Locate every leukocyte (white blood cell).
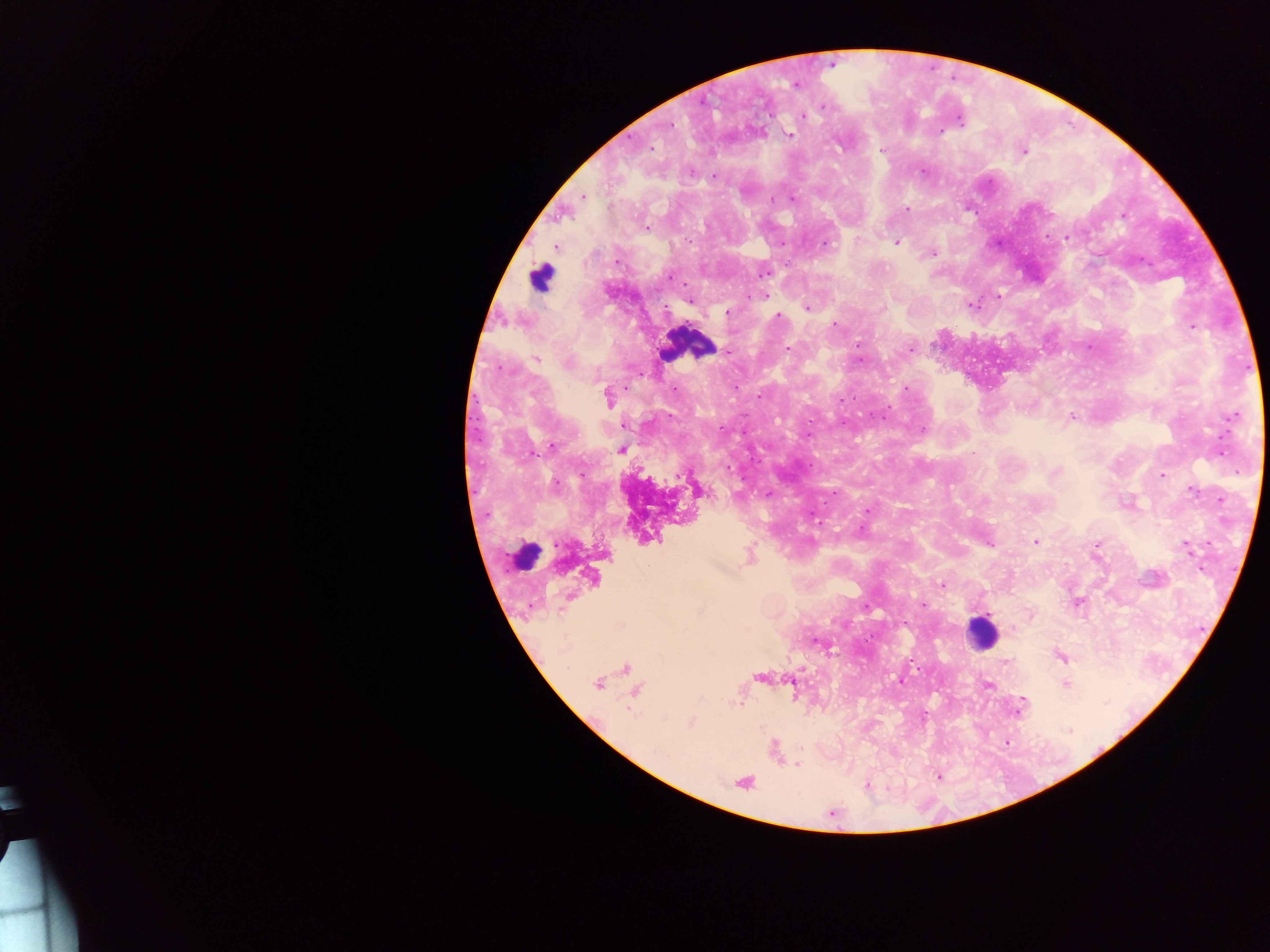
Approximate centers as {x, y} in pixels.
Leukocytes: {540, 278}, {687, 344}, {524, 556}, {981, 631}.

image_size: 1270×952 pixels
capture: mobile-phone photograph through a microscope
preparation: thick blood film
country: Ghana
field_of_view: single
plasmodium_parasite_locations: 'approximate centers as {x, y} in pixels: {830, 65}, {795, 85}, {823, 107}, {803, 116}, {959, 119}, {669, 125}, {939, 131}, {788, 133}, {650, 148}, {882, 149}, {1023, 151}, {713, 177}, {583, 195}, {792, 199}, {907, 209}, {1123, 216}, {646, 227}, {1066, 237}, {897, 242}, {556, 246}, {931, 252}, {765, 295}, {997, 297}, {689, 299}, {971, 305}, {808, 307}, {726, 312}, {777, 316}, {835, 324}, {1192, 326}, {787, 348}, {910, 349}, {727, 351}, {536, 359}, {859, 359}, {499, 368}, {674, 388}, {905, 389}, {607, 396}, {840, 402}, {1235, 415}, {1072, 416}, {844, 423}, {922, 429}, {808, 435}, {551, 448}, {622, 450}, {1162, 475}, {696, 489}, {767, 494}, {867, 511}, {1035, 541}, {988, 544}, {1097, 544}, {1185, 545}, {749, 555}, {942, 584}, {1077, 602}, {923, 605}, {867, 608}, {815, 641}, {1061, 657}, {913, 663}, {1005, 663}, {626, 668}, {759, 676}, {900, 680}, {598, 683}, {986, 684}, {1065, 684}, {635, 691}, {1019, 705}, {691, 722}, {1005, 741}, {775, 751}, {798, 765}, {939, 777}, {743, 782}, {867, 786}'